Report the malaria status of this cell.
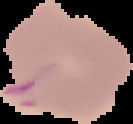

It is parasitized.

Image is 133×124 pixels. From a thin blood film. Cell region segmented out of the field of view; the surrounding area is masked to black.